Report the malaria status of this cell.
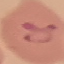
It is parasitized.

Automatically extracted cell patch, resized to 64 × 64 pixels. Photographed with a smartphone camera at the microscope eyepiece. Giemsa-stained preparation. Thin blood smear.